Name the cell type shown.
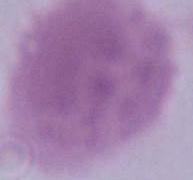

An erythrocyte.

Summary:
  - Magnification: 1000x
  - Modality: micrograph